Identify the parasite.
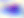
This is Toxoplasma gondii.

Summary:
  - Modality: micrograph
  - Magnification: 400x